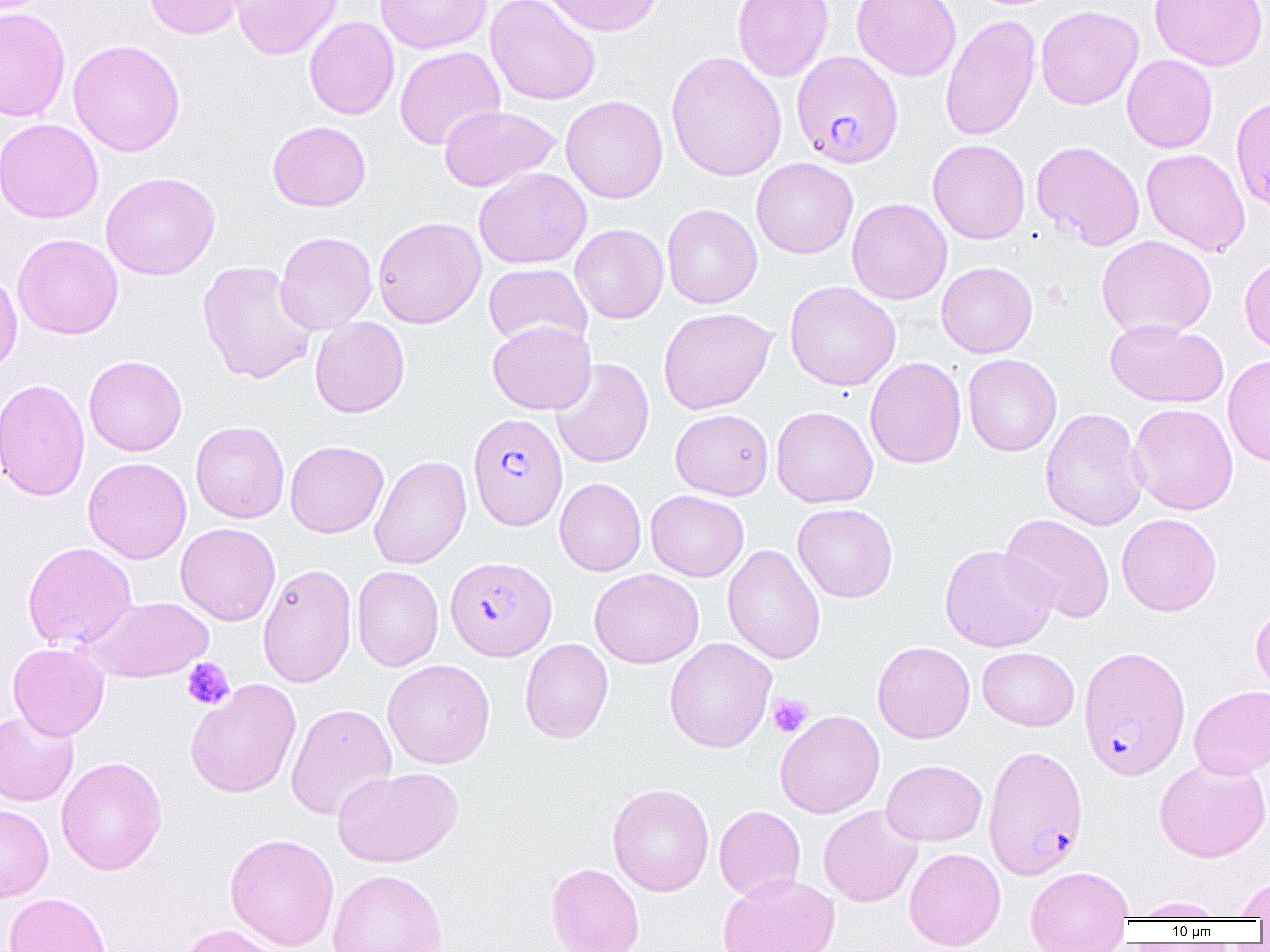

Summary:
  - Coordinate format: approximate bounding boxes as [x1, y1, x2, y2] in pixels
  - Uninfected red blood cell locations: [143, 0, 248, 39], [231, 0, 343, 60], [375, 0, 492, 54], [485, 0, 601, 106], [543, 0, 663, 36], [732, 0, 834, 81], [852, 0, 961, 81], [1150, 0, 1267, 71], [1035, 6, 1143, 110], [0, 8, 71, 122], [940, 14, 1041, 142], [304, 16, 399, 120], [68, 39, 186, 157], [394, 46, 505, 150], [666, 52, 787, 181], [1122, 55, 1218, 153], [1231, 94, 1270, 216], [560, 96, 668, 204], [439, 105, 561, 192], [0, 119, 103, 224], [267, 121, 371, 212], [927, 139, 1030, 244], [1031, 140, 1145, 251], [1142, 148, 1250, 257], [751, 158, 858, 259], [474, 166, 592, 269], [101, 171, 221, 280], [846, 198, 951, 305], [662, 204, 762, 309], [372, 216, 486, 328], [570, 224, 668, 324], [275, 231, 377, 334], [12, 234, 123, 339], [1096, 235, 1217, 339], [1239, 256, 1270, 354], [197, 260, 317, 384], [936, 262, 1038, 358], [955, 262, 1048, 456], [483, 263, 592, 351], [0, 271, 22, 381], [785, 280, 901, 391], [658, 307, 776, 414], [310, 317, 410, 418], [1105, 319, 1228, 408], [487, 320, 597, 414], [963, 354, 1062, 457], [84, 355, 187, 456], [1222, 355, 1270, 467], [864, 357, 967, 469], [551, 358, 654, 468], [1, 378, 90, 501], [1128, 403, 1238, 515], [771, 406, 878, 508], [1040, 407, 1148, 531], [670, 409, 774, 500], [191, 420, 290, 523], [284, 440, 388, 537], [369, 454, 471, 569], [83, 457, 192, 564], [554, 478, 646, 576], [646, 490, 749, 581], [792, 503, 898, 603], [999, 513, 1115, 624], [1116, 513, 1222, 616], [175, 522, 281, 626], [22, 542, 138, 652], [722, 544, 825, 665], [939, 545, 1058, 652], [257, 563, 357, 688], [352, 566, 444, 671], [590, 568, 704, 668], [83, 596, 213, 683], [1250, 603, 1270, 699], [664, 637, 777, 753], [520, 638, 613, 743], [872, 641, 975, 743], [8, 642, 110, 741], [978, 647, 1079, 731], [383, 659, 495, 769], [185, 679, 302, 799], [1189, 685, 1270, 779], [285, 703, 397, 821], [0, 710, 79, 806], [775, 710, 884, 818], [56, 756, 167, 875], [1154, 757, 1270, 862], [881, 759, 987, 846], [332, 766, 462, 868], [607, 783, 714, 896], [0, 804, 54, 903], [714, 804, 805, 901], [819, 805, 923, 907], [225, 833, 339, 950], [904, 847, 1006, 950], [545, 862, 645, 952], [1025, 866, 1133, 951], [328, 868, 448, 952], [717, 873, 839, 952], [1234, 875, 1270, 919], [4, 892, 111, 952], [1129, 897, 1230, 920], [174, 923, 286, 952]
  - Platelet locations: [182, 657, 235, 710], [768, 694, 813, 737]
  - Plasmodium falciparum-infected red blood cell locations: [791, 51, 903, 168], [468, 413, 568, 531], [445, 556, 557, 661], [1083, 644, 1195, 779], [983, 745, 1088, 880]
  - Slide-level diagnosis: Plasmodium falciparum
  - Preparation: thin blood film
  - Image size: 1270×952 pixels
  - Modality: optical microscopy
  - Magnification: 1000x
  - Field of view: one of a larger specimen